Identify the parasite.
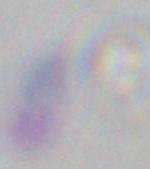

This is Toxoplasma gondii.

1000x magnification. Photomicrograph.